State the blood parasite species.
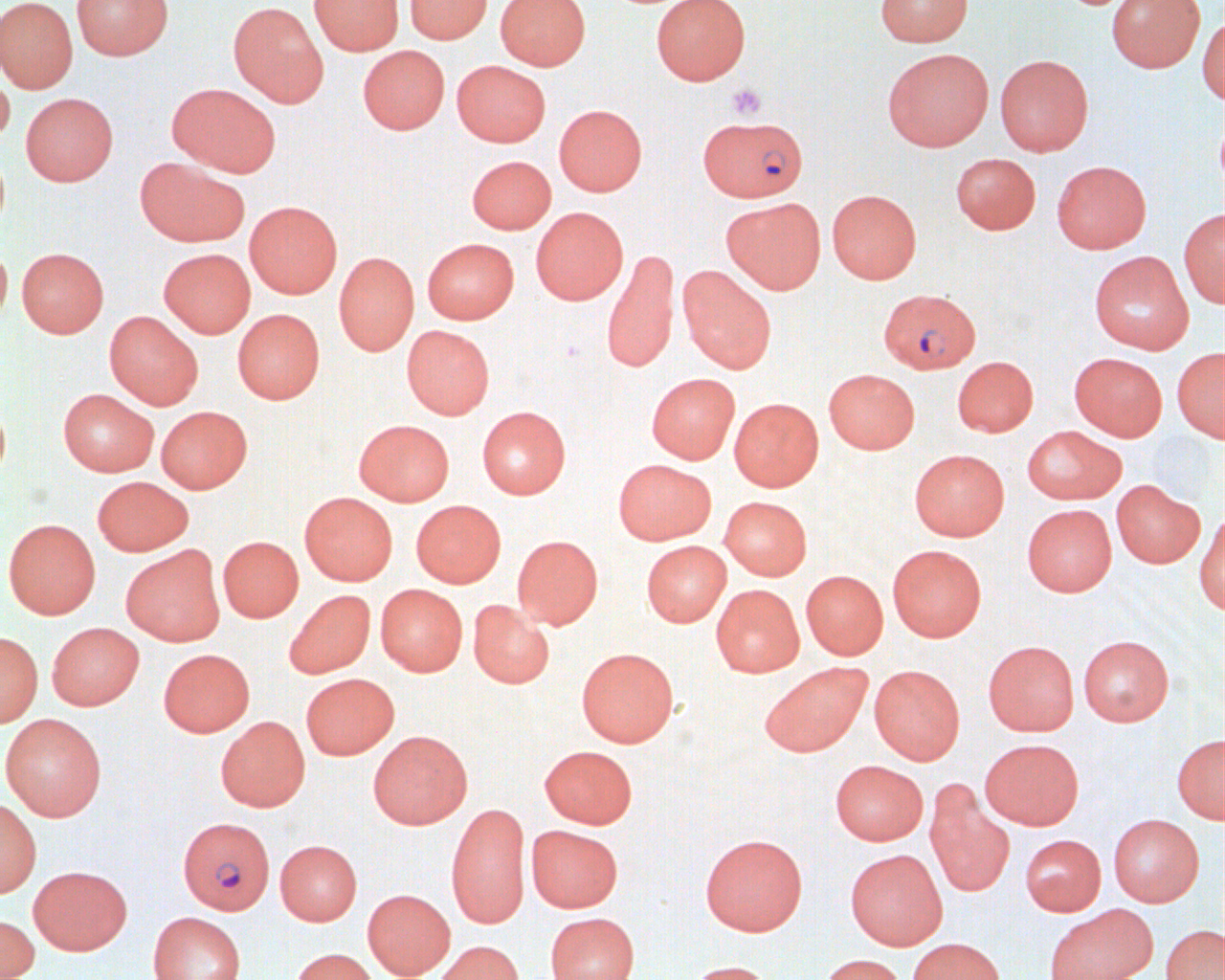

Plasmodium falciparum.

Summary:
  - Coordinate format: approximate bounding boxes as [x1, y1, x2, y2] in pixels
  - Platelet locations: [726, 83, 768, 121]
  - Uninfected red blood cell locations: [0, 0, 78, 93], [71, 0, 173, 60], [309, 0, 403, 55], [405, 0, 491, 44], [495, 0, 589, 69], [651, 0, 750, 85], [875, 0, 972, 46], [1106, 0, 1205, 72], [228, 2, 328, 107], [1197, 13, 1225, 105], [357, 45, 449, 134], [882, 48, 994, 151], [995, 55, 1093, 156], [451, 60, 551, 147], [0, 69, 15, 148], [166, 82, 281, 177], [21, 92, 118, 186], [553, 104, 647, 196], [951, 153, 1041, 234], [466, 155, 556, 234], [134, 156, 250, 247], [1051, 160, 1152, 253], [827, 189, 921, 284], [721, 197, 825, 294], [244, 200, 342, 298], [531, 207, 628, 304], [1179, 208, 1225, 308], [422, 238, 519, 324], [0, 245, 12, 329], [16, 247, 108, 338], [158, 248, 256, 338], [601, 249, 680, 373], [334, 251, 419, 355], [1088, 251, 1194, 355], [678, 266, 777, 374], [233, 309, 325, 404], [104, 311, 203, 409], [402, 325, 495, 419], [1172, 346, 1225, 442], [1069, 352, 1168, 441], [952, 356, 1038, 437], [824, 369, 920, 454], [646, 373, 740, 464], [58, 388, 158, 477], [729, 397, 823, 492], [0, 399, 11, 486], [155, 406, 252, 493], [476, 406, 570, 499], [353, 419, 455, 506], [1022, 426, 1126, 504], [909, 449, 1010, 541], [612, 459, 716, 545], [91, 476, 194, 556], [1111, 479, 1205, 568], [299, 492, 398, 585], [719, 496, 812, 580], [411, 500, 506, 588], [1022, 504, 1116, 597], [1195, 511, 1225, 616], [3, 518, 100, 619], [512, 534, 603, 629], [218, 536, 303, 622], [641, 541, 731, 627], [887, 544, 987, 641], [121, 545, 225, 646], [801, 570, 888, 660], [376, 584, 467, 676], [711, 584, 804, 677], [283, 589, 375, 679], [468, 599, 554, 688], [46, 622, 144, 710], [0, 631, 42, 727], [1077, 635, 1174, 726], [983, 640, 1079, 736], [576, 647, 678, 747], [158, 648, 255, 737], [759, 661, 872, 757], [869, 664, 965, 764], [301, 673, 399, 760], [1, 713, 107, 820], [216, 716, 310, 812], [368, 730, 473, 828], [1172, 732, 1225, 824], [979, 738, 1084, 830], [538, 745, 638, 829], [829, 760, 928, 845], [925, 784, 1014, 898], [0, 798, 41, 898], [446, 802, 531, 929], [1108, 814, 1204, 907], [526, 825, 623, 912], [699, 833, 808, 936], [1020, 834, 1106, 916], [275, 840, 362, 925], [845, 849, 947, 950], [28, 865, 132, 955], [362, 889, 455, 980], [1044, 903, 1158, 980], [147, 912, 246, 980], [545, 912, 639, 980], [0, 914, 39, 980], [1161, 924, 1224, 980], [907, 937, 1005, 980], [434, 940, 525, 980], [289, 948, 379, 980], [818, 954, 908, 980], [683, 960, 777, 980]
  - Plasmodium falciparum-infected red blood cell locations: [701, 118, 811, 205], [879, 287, 980, 374], [182, 818, 280, 917]
  - Field of view: one of a larger specimen
  - Image size: 1225×980 pixels
  - Preparation: thin blood smear
  - Magnification: 1000x
  - Modality: light microscopy